Classify this cell by malaria status.
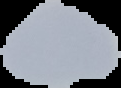

It is uninfected.

Cell region segmented out of the field of view; the surrounding area is masked to black. From a thin blood smear. Image is 121×88 pixels.